Identify the cell.
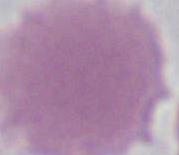
An erythrocyte.

Captured at 1000x magnification. Photomicrograph.